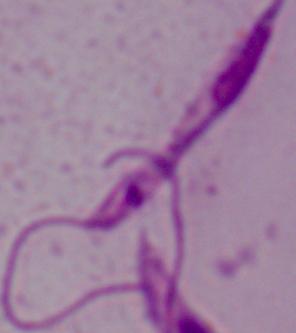

identification = Leishmania
modality = photomicrograph
magnification = 1000x